State which cell type is depicted.
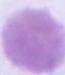
An erythrocyte.

1000x magnification. Micrograph.